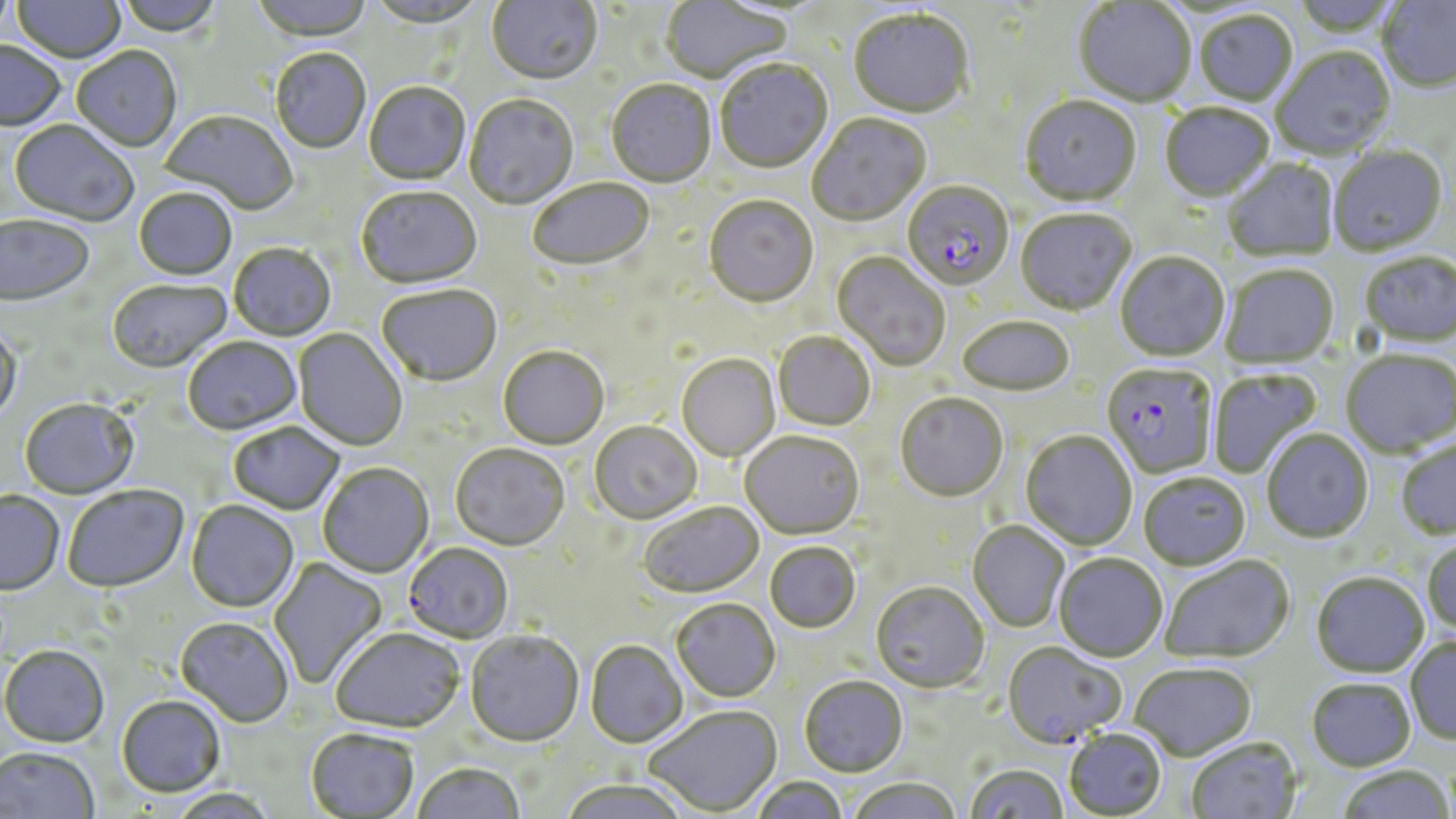
Approximate bounding boxes as (x1,y1)-(x2,y2) corner pairs in pixels. Plasmodium falciparum-infected red blood cell locations: (901,182)-(1013,292), (1101,364)-(1216,479), (403,543)-(514,644), (1002,643)-(1126,750). Uninfected red blood cell locations: (0,0)-(16,45), (12,0)-(126,65), (115,0)-(224,39), (250,0)-(373,44), (487,0)-(602,87), (661,0)-(794,85), (1376,0)-(1456,95), (367,1)-(489,30), (1073,2)-(1196,108), (848,10)-(974,120), (1193,11)-(1298,107), (0,42)-(66,134), (71,48)-(182,153), (1272,48)-(1396,160), (271,50)-(371,155), (715,61)-(834,175), (606,80)-(716,189), (364,83)-(470,186), (464,96)-(578,210), (1020,96)-(1141,209), (1159,104)-(1274,203), (160,111)-(298,216), (807,114)-(931,228), (8,121)-(138,227), (1329,146)-(1448,257), (1223,159)-(1339,263), (528,180)-(655,273), (356,188)-(482,291), (134,190)-(237,281), (704,197)-(818,309), (1015,210)-(1137,317), (1,216)-(95,308), (229,244)-(336,342), (832,253)-(950,372), (1115,253)-(1230,363), (1359,253)-(1456,348), (1219,265)-(1339,370), (107,280)-(232,373), (376,286)-(502,388), (957,317)-(1075,398), (0,325)-(23,426), (293,329)-(408,452), (773,332)-(875,432), (183,337)-(302,435), (498,346)-(609,450), (1340,350)-(1456,458), (677,354)-(780,462), (1208,369)-(1323,480), (895,393)-(1008,503), (19,398)-(139,500), (228,421)-(345,515), (589,422)-(702,525), (1261,429)-(1373,544), (1020,431)-(1137,551), (740,432)-(865,541), (1396,439)-(1456,541), (450,444)-(569,552), (318,463)-(435,578), (1139,474)-(1251,571), (62,485)-(189,592), (0,492)-(64,596), (186,500)-(299,613), (639,502)-(764,599), (967,522)-(1069,634), (1423,538)-(1456,635), (765,542)-(861,634), (1054,554)-(1167,663), (1159,556)-(1295,665), (268,557)-(388,690), (1311,572)-(1429,678), (870,583)-(988,693), (671,598)-(781,703), (175,617)-(294,727), (331,629)-(464,734), (465,631)-(584,748), (1406,636)-(1456,744), (585,641)-(688,749), (0,644)-(110,747), (1130,664)-(1257,762), (799,676)-(908,778), (1306,678)-(1416,772), (117,695)-(226,797), (645,706)-(782,816), (305,729)-(419,818), (1064,729)-(1167,818), (1186,738)-(1303,819), (0,746)-(100,819), (412,763)-(525,819), (965,764)-(1068,819), (1338,765)-(1455,818), (751,776)-(848,819), (846,778)-(962,819), (558,780)-(692,819), (166,788)-(280,818). Slide-level diagnosis: Plasmodium falciparum. Light microscopy. Thin blood film. One field of a larger specimen. Captured at 1000x magnification. May-Grünwald-Giemsa stain. Image is 1456×819 pixels.